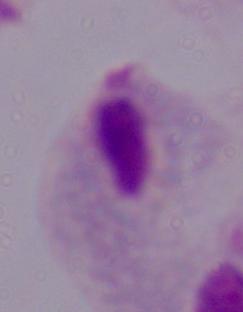
identification = trichomonad
magnification = 1000x
modality = photomicrograph